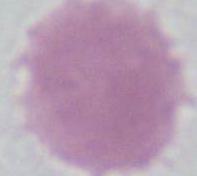
Summary:
  - Modality: photomicrograph
  - Identification: erythrocyte
  - Magnification: 1000x